Locate and identify every blood parasite.
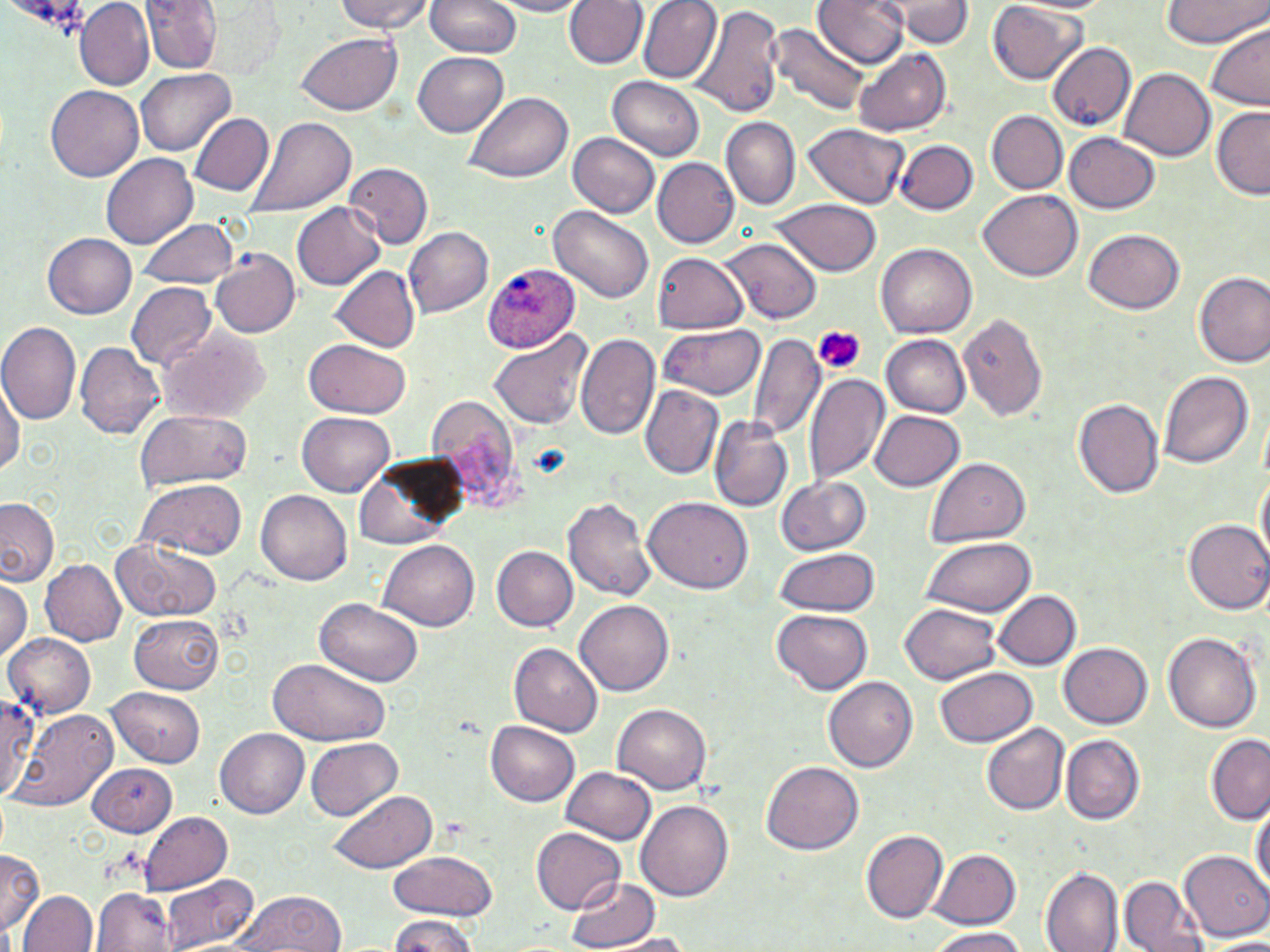
Approximate bounding boxes as [x1, y1, x2, y2] in pixels.
Plasmodium ovale-infected red blood cells: [482, 263, 581, 353].
No Plasmodium falciparum, Plasmodium malariae, Plasmodium vivax, Babesia divergens, or Trypanosoma brucei observed.

Platelet locations: [816, 326, 866, 375]. Uninfected red blood cell locations: [76, 0, 155, 90], [334, 0, 435, 33], [425, 0, 519, 58], [489, 0, 589, 17], [564, 0, 649, 71], [637, 0, 722, 83], [812, 0, 911, 68], [1159, 0, 1270, 46], [140, 1, 227, 75], [882, 1, 974, 47], [202, 3, 281, 77], [987, 3, 1086, 84], [694, 4, 786, 120], [771, 23, 870, 118], [1206, 25, 1270, 112], [295, 32, 402, 115], [1049, 43, 1137, 129], [853, 47, 952, 137], [413, 53, 509, 137], [1121, 67, 1216, 163], [137, 68, 235, 156], [608, 75, 706, 162], [44, 84, 143, 182], [464, 91, 572, 182], [1212, 105, 1269, 198], [987, 111, 1068, 194], [189, 113, 274, 195], [721, 115, 799, 210], [247, 116, 357, 218], [803, 124, 909, 209], [1063, 131, 1161, 214], [568, 132, 659, 217], [896, 141, 977, 215], [101, 154, 197, 246], [652, 157, 739, 247], [343, 161, 433, 248], [979, 189, 1082, 281], [769, 199, 883, 277], [293, 203, 386, 290], [548, 205, 654, 303], [138, 217, 239, 288], [405, 227, 493, 317], [1085, 228, 1185, 314], [43, 233, 136, 319], [718, 237, 822, 325], [877, 243, 977, 338], [210, 247, 301, 338], [650, 252, 748, 334], [331, 266, 420, 350], [1194, 269, 1270, 368], [126, 281, 216, 370], [958, 314, 1049, 422], [0, 320, 83, 423], [659, 324, 765, 401], [155, 325, 274, 423], [812, 325, 863, 380], [488, 328, 592, 433], [575, 333, 658, 440], [747, 333, 825, 442], [881, 335, 971, 417], [303, 336, 412, 417], [74, 341, 165, 439], [710, 361, 818, 494], [1157, 370, 1254, 469], [803, 371, 892, 486], [0, 377, 23, 474], [639, 384, 723, 480], [425, 394, 529, 516], [1074, 398, 1164, 499], [1258, 400, 1270, 484], [134, 409, 254, 494], [870, 410, 965, 489], [297, 412, 395, 497], [708, 415, 794, 513], [354, 455, 464, 549], [927, 457, 1031, 547], [1254, 466, 1270, 569], [776, 475, 872, 556], [136, 479, 247, 559], [256, 490, 353, 585], [642, 495, 753, 594], [562, 497, 656, 602], [0, 498, 58, 587], [1183, 519, 1270, 613], [919, 538, 1035, 616], [379, 539, 478, 630], [111, 540, 222, 623], [492, 546, 577, 630], [774, 548, 880, 616], [40, 559, 127, 646], [0, 576, 32, 660], [993, 590, 1082, 670], [316, 598, 423, 686], [576, 598, 673, 695], [899, 603, 1003, 684], [773, 608, 873, 693], [130, 614, 223, 693], [1164, 632, 1261, 732], [5, 633, 96, 717], [508, 642, 604, 735], [1060, 643, 1152, 728], [267, 659, 388, 747], [935, 667, 1039, 746], [823, 675, 918, 772], [108, 687, 206, 767], [0, 695, 39, 794], [614, 703, 712, 794], [12, 710, 117, 811], [486, 721, 580, 805], [981, 722, 1070, 815], [215, 727, 308, 817], [1062, 734, 1145, 825], [1206, 735, 1270, 823], [306, 737, 404, 822], [762, 760, 864, 854], [88, 763, 178, 836], [563, 767, 657, 843], [327, 790, 436, 874], [1250, 799, 1269, 893], [638, 802, 733, 902], [138, 812, 232, 895], [532, 825, 626, 914], [860, 828, 948, 925], [930, 848, 1021, 929], [0, 849, 43, 938], [1179, 849, 1270, 942], [387, 850, 497, 919], [1042, 869, 1123, 951], [158, 874, 259, 952], [566, 875, 660, 951], [1119, 876, 1207, 952], [91, 888, 174, 951], [19, 891, 100, 952], [230, 891, 345, 950], [387, 914, 481, 951], [926, 927, 1031, 952], [600, 934, 699, 951], [1204, 938, 1270, 951]. Slide-level diagnosis: Plasmodium ovale. Thin blood smear. Optical microscopy. Image is 1270×952 pixels. May-Grünwald-Giemsa-stained preparation. One field of a larger specimen. Captured at 1000x magnification.